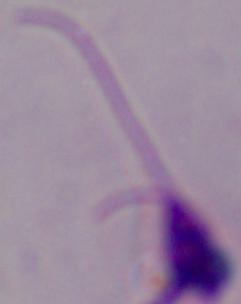
magnification = 1000x
modality = micrograph
identification = Leishmania